Name the blood parasite species.
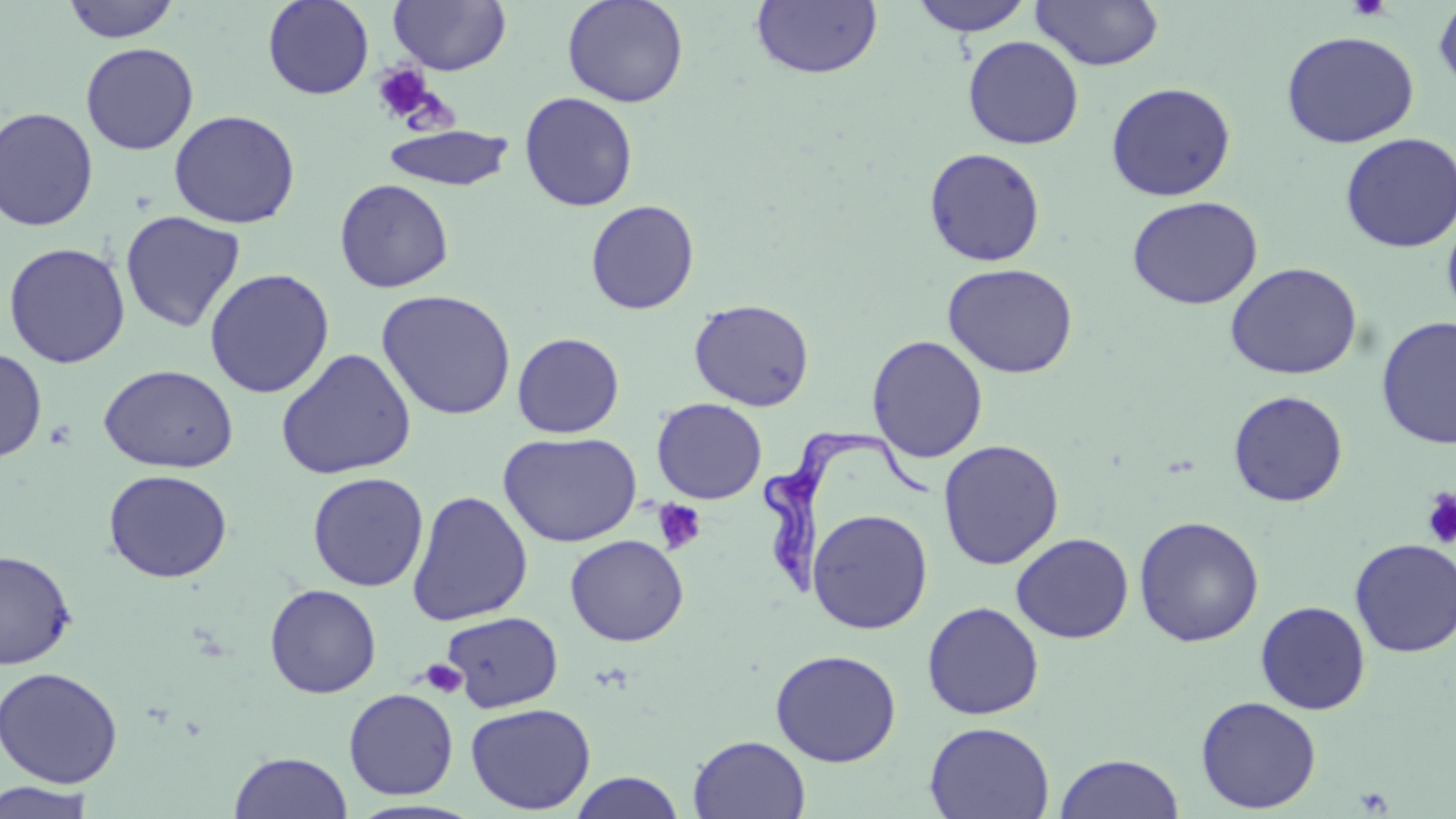
Trypanosoma brucei.

Summary:
  - Coordinate format: approximate bounding boxes as [x1, y1, x2, y2] in pixels
  - Trypanosoma brucei locations: [762, 425, 930, 592]
  - Uninfected red blood cell locations: [62, 0, 181, 43], [262, 0, 375, 100], [389, 0, 511, 75], [561, 0, 689, 108], [909, 0, 1035, 36], [1030, 0, 1164, 70], [1432, 0, 1456, 99], [750, 1, 884, 80], [1280, 30, 1419, 148], [962, 35, 1084, 149], [80, 42, 199, 155], [1105, 81, 1237, 201], [519, 91, 639, 212], [0, 107, 99, 232], [168, 109, 301, 229], [382, 124, 514, 192], [1340, 132, 1456, 253], [923, 147, 1046, 267], [334, 179, 454, 293], [1127, 195, 1263, 310], [585, 199, 700, 315], [1442, 209, 1456, 324], [120, 210, 246, 333], [3, 242, 131, 368], [942, 262, 1079, 378], [1224, 262, 1363, 380], [203, 268, 335, 398], [376, 290, 517, 420], [689, 298, 814, 411], [1376, 316, 1455, 450], [512, 332, 625, 438], [866, 334, 988, 463], [0, 347, 47, 463], [275, 348, 417, 479], [98, 364, 238, 473], [1228, 390, 1348, 507], [651, 398, 767, 504], [498, 431, 642, 547], [938, 439, 1064, 569], [102, 468, 232, 583], [307, 471, 429, 592], [407, 490, 533, 627], [807, 508, 933, 634], [1133, 515, 1265, 647], [1010, 532, 1134, 644], [565, 534, 688, 646], [1349, 538, 1456, 657], [0, 549, 77, 670], [264, 583, 382, 699], [922, 601, 1044, 720], [1255, 601, 1371, 715], [442, 611, 563, 711], [770, 648, 902, 767], [0, 666, 123, 787], [343, 688, 459, 800], [1195, 696, 1321, 814], [465, 702, 596, 814], [924, 721, 1055, 818], [688, 734, 811, 819], [229, 751, 352, 818], [1054, 753, 1184, 819], [567, 771, 685, 818], [1, 780, 98, 818]
  - Platelet locations: [1347, 0, 1392, 20], [372, 63, 433, 122], [1422, 489, 1456, 549], [653, 500, 707, 554], [421, 659, 468, 698]
  - Image size: 1456×819 pixels
  - Preparation: thin blood film
  - Magnification: 1000x
  - Field of view: one of a larger specimen
  - Modality: light microscopy
  - Stain: May-Grünwald-Giemsa